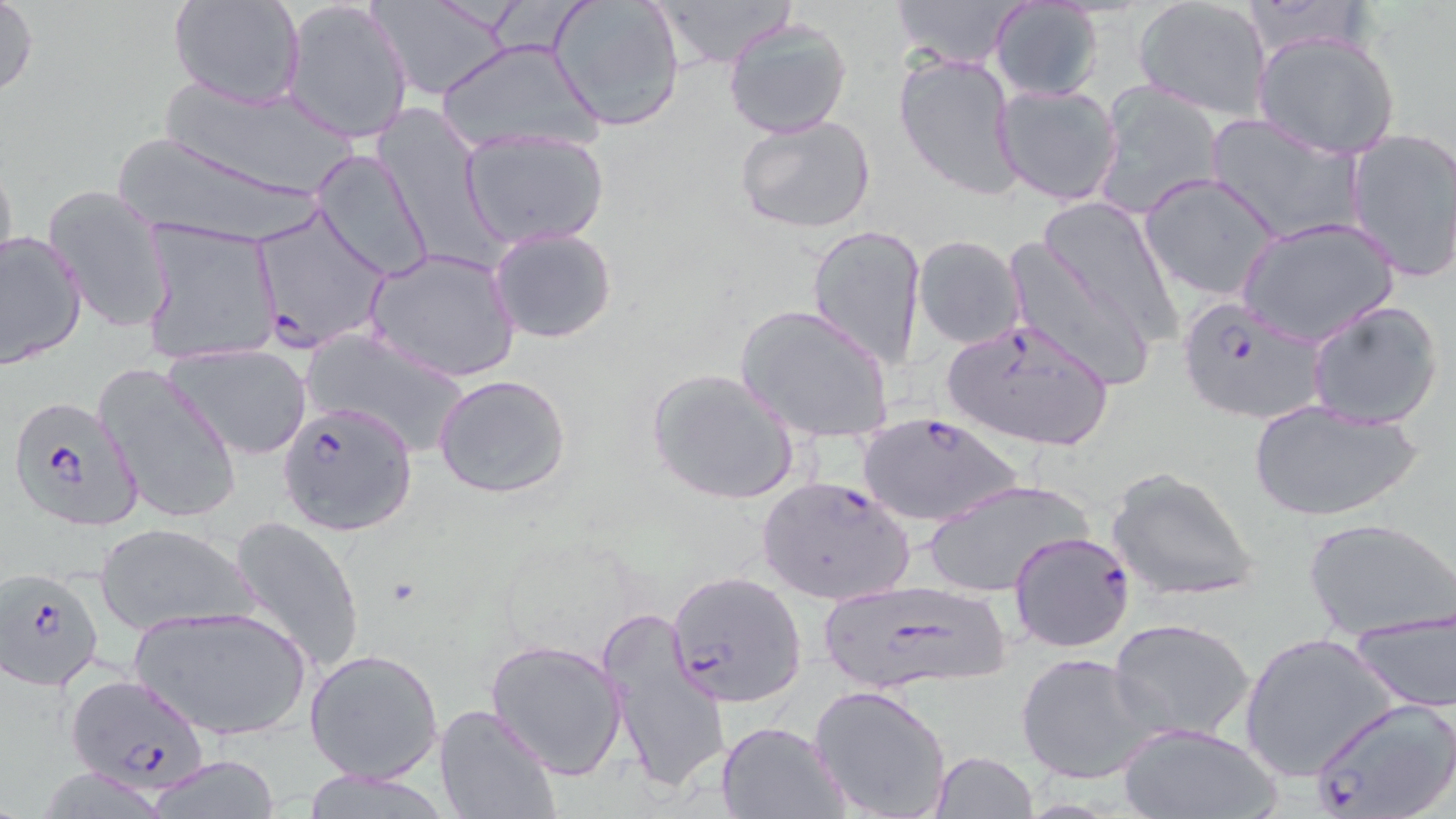
Approximate bounding boxes as (x1,y1)-(x2,y2) corner pairs in pixels. Uninfected red blood cell locations: (170,0)-(305,109), (283,0)-(415,145), (370,0)-(509,100), (547,0)-(686,132), (649,0)-(797,69), (892,0)-(1021,73), (1132,0)-(1274,121), (0,1)-(40,104), (987,1)-(1105,103), (723,17)-(853,139), (1252,29)-(1403,160), (434,38)-(603,159), (894,53)-(1022,200), (156,77)-(360,202), (1091,81)-(1224,220), (993,82)-(1124,208), (735,113)-(877,235), (1205,114)-(1363,245), (461,128)-(610,248), (1343,128)-(1456,283), (116,141)-(329,245), (312,149)-(433,283), (0,153)-(21,284), (1137,172)-(1285,303), (41,183)-(173,333), (1039,196)-(1180,339), (1238,216)-(1400,347), (140,221)-(280,366), (807,224)-(925,369), (488,226)-(618,346), (0,228)-(88,368), (912,234)-(1026,349), (1003,238)-(1161,391), (365,248)-(521,382), (1306,299)-(1446,430), (735,303)-(894,445), (302,332)-(473,457), (164,342)-(314,461), (96,361)-(243,528), (645,366)-(802,507), (433,375)-(572,500), (1247,399)-(1422,523), (1106,467)-(1260,603), (923,477)-(1093,599), (228,514)-(366,675), (1304,516)-(1456,642), (96,522)-(258,636), (130,602)-(311,743), (1345,609)-(1456,714), (599,610)-(729,797), (1109,617)-(1256,742), (1240,631)-(1399,782), (485,638)-(627,778), (303,646)-(445,783), (1016,653)-(1159,786), (809,684)-(951,818), (434,702)-(563,819), (718,721)-(847,817), (1117,722)-(1280,819), (929,751)-(1038,818), (142,758)-(286,817), (301,769)-(452,819). Plasmodium falciparum-infected red blood cell locations: (249,207)-(389,353), (1176,296)-(1328,424), (938,315)-(1115,452), (10,397)-(145,532), (277,400)-(418,537), (857,411)-(1024,528), (754,473)-(916,608), (1010,529)-(1135,652), (1,566)-(106,689), (667,569)-(807,707), (818,579)-(1015,696), (66,671)-(211,793), (1307,698)-(1456,819). Slide-level diagnosis: Plasmodium falciparum. Single field of view. Thin blood film. Optical microscopy. Image is 1456×819 pixels. May-Grünwald-Giemsa-stained preparation. Captured at 1000x magnification.